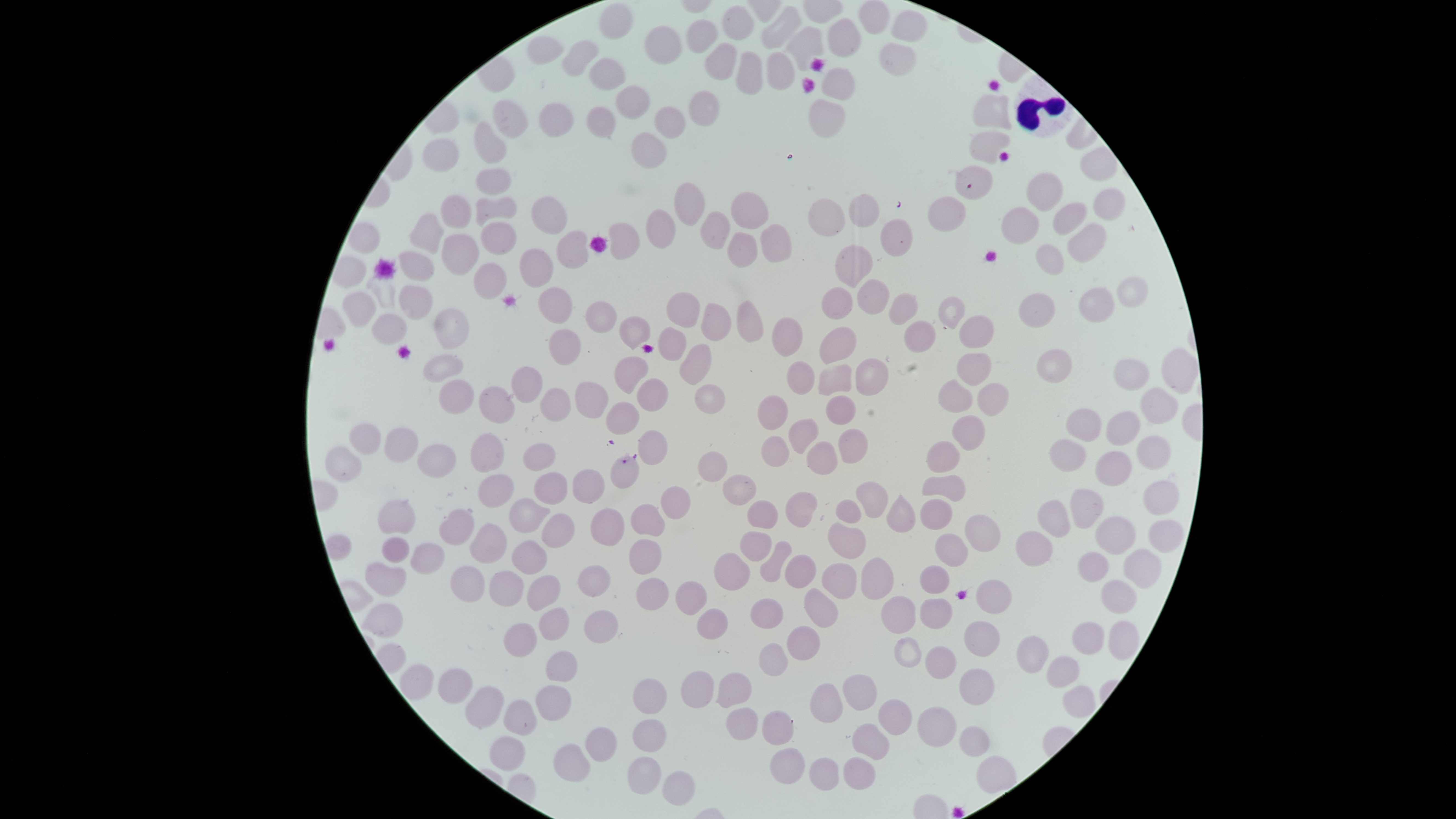
image_size: 1456×819 pixels
white_blood_cells: 'approximate bounding boxes as {left, top, right, bottom} in pixels: {1013, 73, 1074, 138}'
visible_region: circular
preparation: thin smear of blood
capture: smartphone photograph through the microscope eyepiece
stain: Giemsa
field_of_view: single
uninfected_red_blood_cells: 'approximate bounding boxes as {left, top, right, bottom} in pixels: {860, 1, 890, 35}, {600, 3, 635, 39}, {762, 5, 801, 49}, {722, 6, 755, 40}, {889, 10, 927, 42}, {829, 18, 861, 58}, {688, 20, 720, 53}, {645, 25, 681, 63}, {787, 26, 824, 71}, {528, 35, 563, 65}, {561, 39, 601, 77}, {703, 41, 738, 80}, {879, 43, 916, 76}, {734, 51, 764, 94}, {766, 52, 796, 89}, {590, 57, 625, 92}, {822, 67, 855, 102}, {616, 85, 650, 120}, {687, 90, 721, 127}, {973, 94, 1012, 130}, {808, 98, 845, 139}, {494, 99, 529, 139}, {537, 103, 573, 137}, {586, 106, 616, 138}, {654, 106, 687, 139}, {475, 121, 508, 165}, {631, 131, 665, 169}, {970, 132, 1010, 164}, {422, 137, 460, 171}, {1079, 146, 1117, 181}, {955, 166, 993, 200}, {474, 168, 512, 194}, {1026, 171, 1063, 210}, {674, 182, 705, 227}, {1092, 187, 1126, 221}, {731, 191, 770, 229}, {441, 193, 473, 229}, {849, 193, 880, 228}, {927, 195, 967, 231}, {531, 196, 567, 235}, {808, 197, 846, 236}, {475, 198, 516, 225}, {1052, 203, 1087, 235}, {1002, 207, 1040, 244}, {646, 209, 678, 248}, {700, 210, 730, 249}, {407, 213, 445, 254}, {880, 218, 913, 260}, {348, 221, 380, 253}, {481, 221, 517, 255}, {609, 222, 640, 259}, {761, 223, 793, 264}, {1068, 224, 1106, 264}, {556, 231, 589, 269}, {727, 231, 758, 268}, {442, 234, 479, 275}, {834, 244, 874, 288}, {1036, 244, 1064, 276}, {519, 248, 555, 288}, {398, 250, 435, 281}, {474, 263, 508, 299}, {1116, 276, 1149, 310}, {857, 279, 890, 314}, {400, 285, 433, 320}, {822, 286, 853, 319}, {537, 287, 573, 324}, {1079, 287, 1115, 323}, {342, 291, 377, 328}, {666, 291, 700, 326}, {889, 293, 918, 325}, {1018, 293, 1056, 328}, {937, 294, 966, 329}, {736, 300, 763, 344}, {585, 301, 617, 332}, {700, 302, 731, 342}, {434, 309, 471, 350}, {372, 314, 408, 346}, {617, 315, 652, 350}, {958, 315, 995, 347}, {772, 317, 802, 358}, {904, 319, 936, 353}, {820, 326, 856, 365}, {657, 328, 688, 360}, {549, 330, 581, 364}, {680, 343, 712, 384}, {1038, 348, 1072, 383}, {1161, 348, 1199, 393}, {957, 352, 992, 389}, {423, 355, 464, 381}, {614, 356, 650, 393}, {855, 358, 888, 396}, {1115, 359, 1150, 390}, {786, 360, 816, 395}, {818, 364, 853, 396}, {512, 367, 543, 404}, {636, 377, 668, 412}, {938, 379, 973, 414}, {437, 380, 474, 414}, {575, 382, 608, 420}, {978, 382, 1011, 416}, {694, 384, 726, 414}, {479, 385, 515, 424}, {1140, 387, 1177, 424}, {538, 389, 571, 422}, {758, 394, 789, 431}, {825, 395, 857, 425}, {606, 402, 639, 435}, {1066, 408, 1102, 441}, {1106, 411, 1141, 447}, {951, 415, 985, 451}, {788, 418, 818, 453}, {348, 424, 382, 455}, {383, 426, 418, 462}, {838, 428, 869, 463}, {638, 429, 668, 466}, {470, 433, 506, 472}, {1136, 434, 1171, 470}, {760, 435, 790, 467}, {1049, 439, 1087, 473}, {926, 440, 960, 472}, {807, 441, 838, 475}, {521, 443, 555, 471}, {326, 445, 361, 482}, {416, 445, 456, 479}, {697, 451, 728, 483}, {1096, 451, 1132, 486}, {610, 456, 639, 489}, {572, 468, 607, 503}, {533, 472, 569, 505}, {723, 473, 757, 505}, {478, 475, 517, 507}, {922, 475, 965, 500}, {856, 481, 889, 518}, {1143, 481, 1180, 516}, {661, 485, 691, 520}, {1069, 489, 1105, 529}, {785, 491, 818, 529}, {886, 493, 916, 532}, {510, 497, 551, 534}, {747, 498, 777, 528}, {921, 498, 953, 530}, {378, 499, 415, 534}, {836, 500, 862, 522}, {1037, 500, 1071, 539}, {630, 503, 665, 537}, {591, 508, 626, 548}, {440, 509, 474, 547}, {542, 513, 575, 549}, {965, 515, 1001, 552}, {1095, 515, 1136, 555}, {1149, 520, 1185, 552}, {469, 522, 506, 563}, {828, 523, 866, 559}, {1015, 530, 1054, 567}, {739, 531, 771, 562}, {936, 533, 969, 567}, {382, 537, 410, 562}, {629, 539, 662, 576}, {511, 540, 548, 575}, {761, 541, 792, 583}, {409, 543, 445, 574}, {1124, 549, 1162, 589}, {1078, 551, 1109, 582}, {714, 552, 748, 591}, {785, 554, 817, 588}, {366, 562, 406, 597}, {822, 563, 857, 599}, {578, 565, 610, 597}, {919, 565, 950, 594}, {451, 566, 485, 602}, {490, 571, 524, 607}, {527, 575, 560, 611}, {637, 577, 669, 611}, {976, 580, 1012, 614}, {1102, 580, 1138, 614}, {676, 581, 707, 615}, {804, 587, 837, 628}, {881, 596, 916, 634}, {751, 598, 784, 629}, {921, 598, 952, 628}, {360, 603, 404, 636}, {539, 607, 569, 641}, {697, 609, 728, 639}, {583, 610, 619, 642}, {964, 620, 1000, 657}, {1108, 620, 1140, 661}, {1073, 622, 1105, 656}, {503, 623, 537, 657}, {788, 625, 820, 661}, {1016, 637, 1049, 675}, {759, 643, 789, 676}, {546, 651, 578, 681}, {1047, 654, 1080, 688}, {400, 664, 434, 700}, {437, 668, 475, 704}, {959, 669, 994, 706}, {680, 670, 714, 709}, {717, 673, 752, 707}, {632, 678, 667, 715}, {1063, 684, 1096, 718}, {536, 685, 572, 721}, {464, 686, 504, 728}, {503, 700, 537, 736}, {727, 708, 758, 741}, {918, 708, 956, 747}, {762, 710, 794, 745}, {631, 719, 667, 752}, {960, 726, 991, 756}, {585, 727, 617, 761}, {491, 736, 525, 772}, {553, 744, 590, 782}, {771, 748, 806, 784}, {627, 756, 661, 795}, {977, 756, 1016, 795}, {664, 771, 695, 805}'
presence: no malaria parasites detected